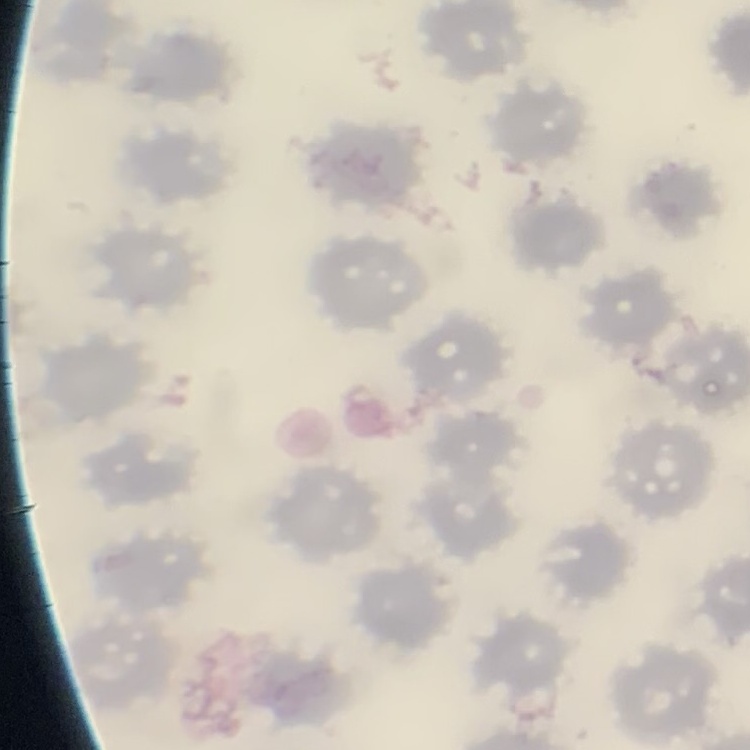

The erythrocytes show no rouleaux formation. Square crop of a larger photomicrograph. Thin blood film. Stained with either Field's or Giemsa.